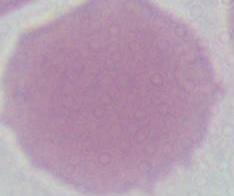
modality = micrograph
magnification = 1000x
identification = red blood cell